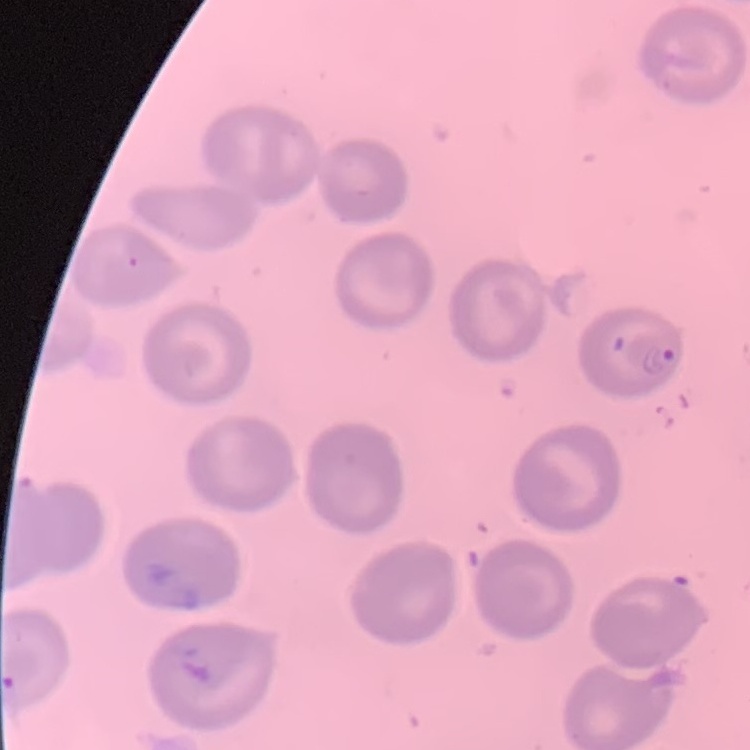

Summary:
  - Red blood cell morphology: no rouleaux formation
  - Preparation: thin peripheral smear
  - Stain: Field's or Giemsa
  - Image type: square crop of a larger photomicrograph